Classify this cell by malaria status.
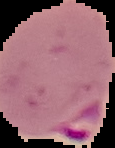

Parasitized.

Summary:
  - Preparation: thin blood film
  - Image size: 115×148 pixels
  - Image type: segmented cell region with the area outside set to black